Give the extent of all Plasmodium falciparum-infected red blood cells.
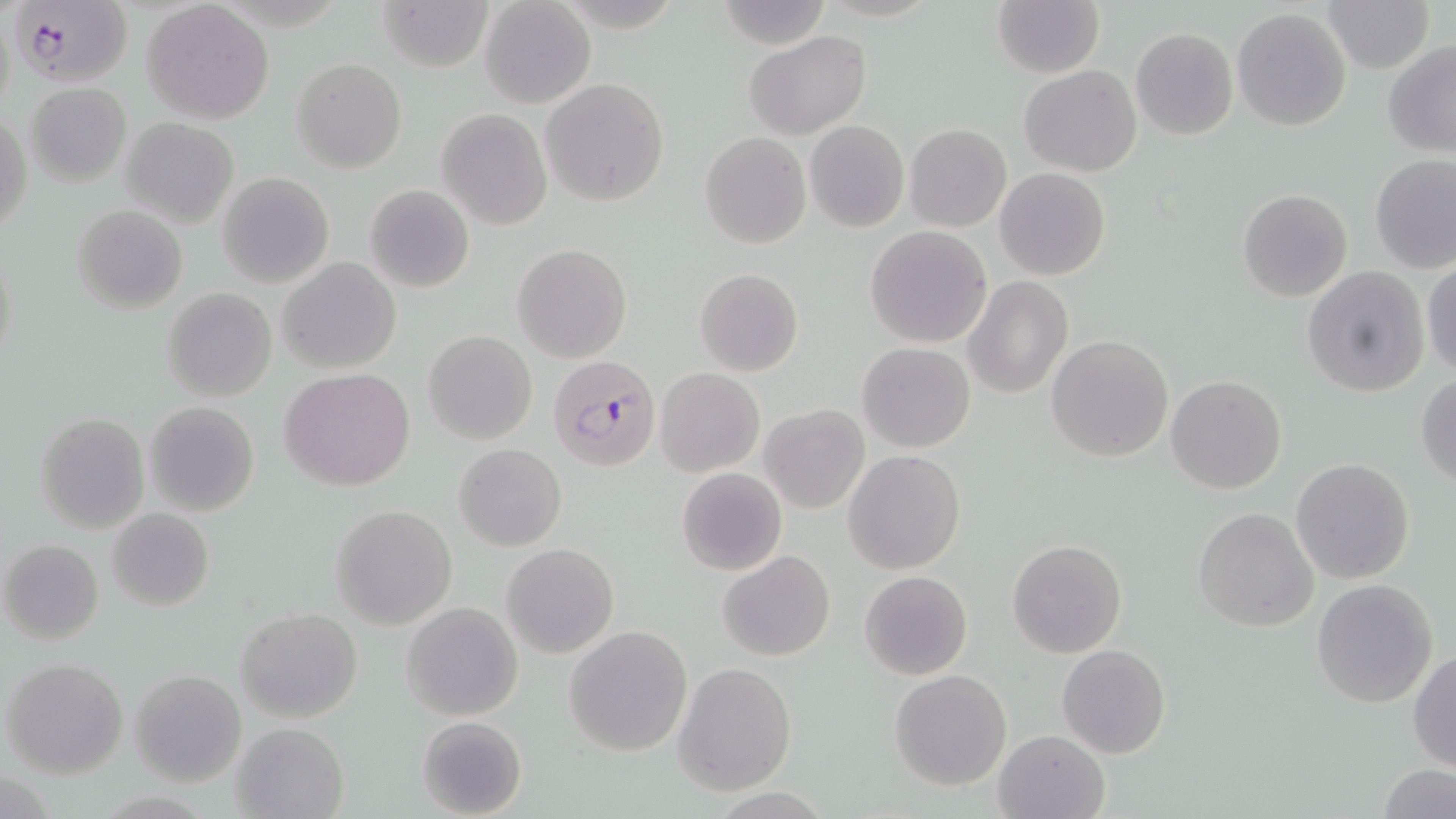
Approximate bounding boxes as named x1/y1/x2/y2 corners in pixels.
Plasmodium falciparum-infected red blood cells: (x1=13, y1=0, x2=137, y2=90), (x1=548, y1=355, x2=661, y2=472).

slide-level diagnosis = Plasmodium falciparum
preparation = thin blood film
stain = May-Grünwald-Giemsa
magnification = 1000x
image size = 1456×819 pixels
modality = optical microscopy
field of view = one of a larger specimen
uninfected red blood cell locations = approximate bounding boxes as named x1/y1/x2/y2 corners in pixels: (x1=376, y1=0, x2=493, y2=71), (x1=1320, y1=0, x2=1433, y2=73), (x1=480, y1=1, x2=595, y2=109), (x1=716, y1=1, x2=834, y2=51), (x1=141, y1=2, x2=276, y2=123), (x1=994, y1=2, x2=1103, y2=77), (x1=1232, y1=7, x2=1354, y2=131), (x1=1130, y1=27, x2=1237, y2=139), (x1=744, y1=31, x2=871, y2=140), (x1=1383, y1=40, x2=1456, y2=158), (x1=291, y1=57, x2=407, y2=173), (x1=1020, y1=65, x2=1143, y2=177), (x1=540, y1=78, x2=671, y2=207), (x1=25, y1=82, x2=131, y2=187), (x1=436, y1=109, x2=550, y2=230), (x1=1, y1=111, x2=31, y2=236), (x1=119, y1=118, x2=239, y2=227), (x1=804, y1=120, x2=909, y2=232), (x1=905, y1=124, x2=1012, y2=232), (x1=700, y1=131, x2=811, y2=249), (x1=1369, y1=155, x2=1456, y2=274), (x1=994, y1=167, x2=1110, y2=280), (x1=217, y1=172, x2=334, y2=288), (x1=365, y1=184, x2=475, y2=294), (x1=1237, y1=189, x2=1353, y2=302), (x1=71, y1=204, x2=187, y2=314), (x1=865, y1=225, x2=993, y2=349), (x1=514, y1=244, x2=633, y2=363), (x1=276, y1=258, x2=401, y2=373), (x1=1422, y1=260, x2=1456, y2=379), (x1=1302, y1=264, x2=1430, y2=397), (x1=696, y1=267, x2=803, y2=377), (x1=963, y1=275, x2=1073, y2=399), (x1=162, y1=288, x2=277, y2=403), (x1=909, y1=302, x2=1030, y2=428), (x1=424, y1=330, x2=537, y2=445), (x1=1046, y1=334, x2=1174, y2=462), (x1=858, y1=342, x2=976, y2=452), (x1=279, y1=368, x2=416, y2=491), (x1=656, y1=368, x2=765, y2=477), (x1=1415, y1=372, x2=1456, y2=489), (x1=1166, y1=374, x2=1287, y2=495), (x1=143, y1=402, x2=259, y2=516), (x1=760, y1=403, x2=868, y2=512), (x1=35, y1=412, x2=150, y2=534), (x1=454, y1=443, x2=567, y2=551), (x1=844, y1=450, x2=966, y2=574), (x1=1290, y1=458, x2=1415, y2=585), (x1=676, y1=467, x2=787, y2=577), (x1=330, y1=504, x2=458, y2=628), (x1=1192, y1=507, x2=1319, y2=633), (x1=107, y1=508, x2=214, y2=611), (x1=1008, y1=539, x2=1126, y2=657), (x1=1, y1=540, x2=104, y2=644), (x1=502, y1=542, x2=618, y2=657), (x1=718, y1=551, x2=835, y2=660), (x1=859, y1=570, x2=973, y2=680), (x1=1311, y1=578, x2=1439, y2=707), (x1=402, y1=603, x2=523, y2=721), (x1=236, y1=608, x2=363, y2=724), (x1=563, y1=624, x2=693, y2=756), (x1=1057, y1=644, x2=1171, y2=760), (x1=1408, y1=650, x2=1456, y2=771), (x1=2, y1=657, x2=127, y2=779), (x1=673, y1=662, x2=797, y2=794), (x1=130, y1=669, x2=248, y2=786), (x1=889, y1=670, x2=1012, y2=791), (x1=415, y1=715, x2=527, y2=819), (x1=229, y1=722, x2=349, y2=819), (x1=992, y1=730, x2=1109, y2=819), (x1=1377, y1=765, x2=1455, y2=819)